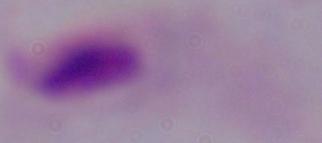

Photomicrograph. A trichomonad is shown. 1000x magnification.